Outline each Plasmodium falciparum-infected red blood cell.
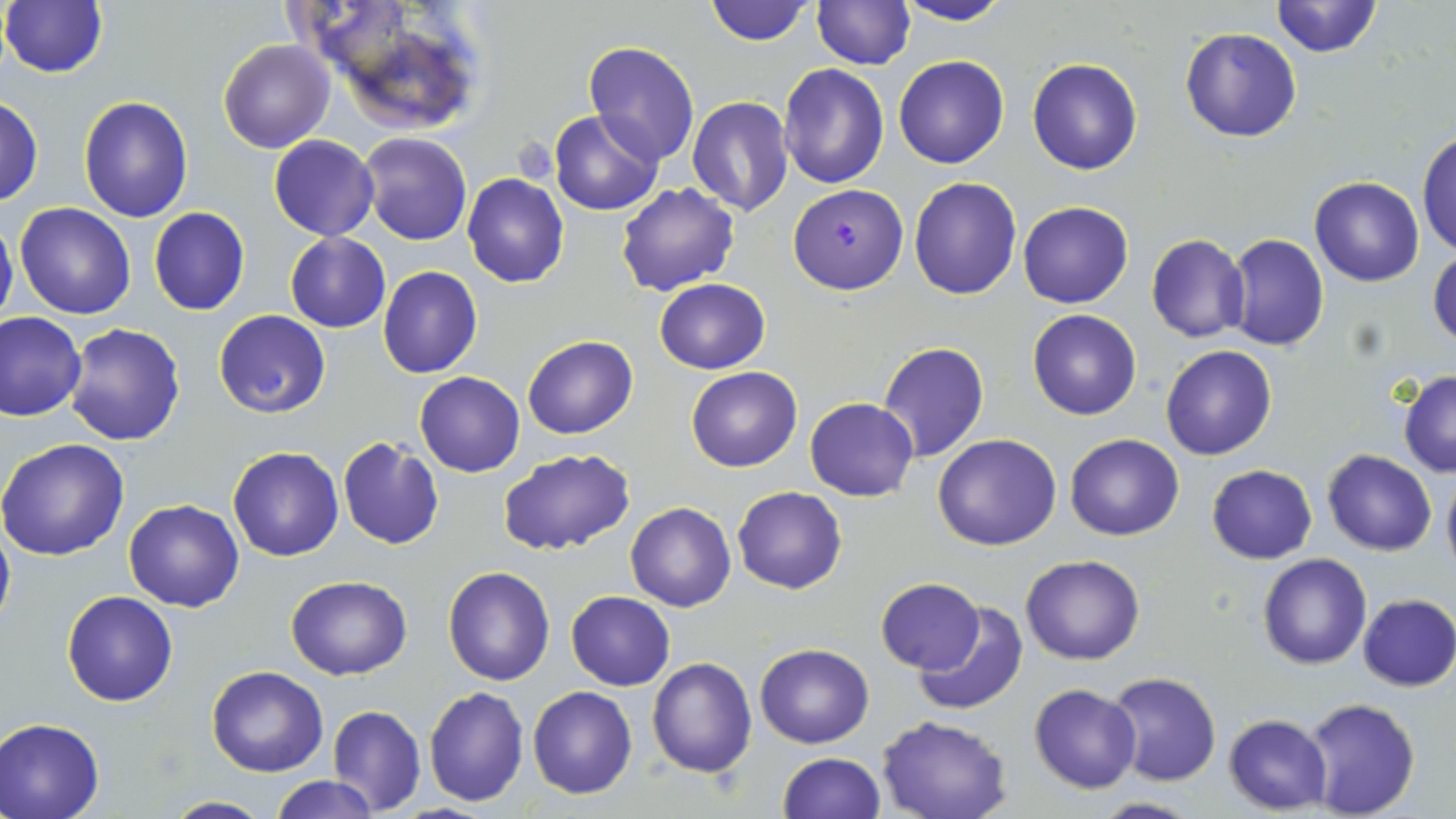

Approximate bounding boxes as (x1,y1)-(x2,y2) corner pairs in pixels.
Plasmodium falciparum-infected red blood cells: (787,183)-(908,294).

Summary:
  - Uninfected red blood cell locations: (704,0)-(815,46), (1269,0)-(1384,57), (895,1)-(1013,27), (1,2)-(108,78), (812,2)-(914,69), (315,6)-(492,135), (1180,26)-(1302,142), (218,39)-(334,153), (582,41)-(700,167), (893,56)-(1009,170), (1027,57)-(1143,175), (779,63)-(888,188), (0,95)-(44,206), (78,96)-(194,223), (685,97)-(795,218), (550,110)-(663,215), (1416,127)-(1456,259), (358,132)-(472,245), (269,135)-(379,240), (462,174)-(569,289), (908,175)-(1023,300), (1309,176)-(1425,286), (616,182)-(741,296), (14,201)-(137,320), (1018,201)-(1134,309), (148,208)-(251,316), (0,212)-(18,331), (285,232)-(390,331), (1146,234)-(1251,343), (1225,234)-(1330,351), (1429,246)-(1456,350), (378,267)-(483,379), (654,279)-(772,375), (1027,308)-(1141,420), (214,309)-(331,418), (0,311)-(85,421), (62,323)-(186,446), (521,335)-(638,439), (878,342)-(990,462), (1160,346)-(1278,461), (686,366)-(802,472), (1398,369)-(1456,477), (415,372)-(525,476), (805,397)-(918,502), (933,432)-(1061,550), (1064,432)-(1184,541), (336,436)-(444,550), (0,437)-(131,559), (227,447)-(344,561), (498,447)-(636,556), (1322,450)-(1438,556), (1206,464)-(1318,564), (1440,464)-(1456,580), (733,486)-(848,594), (124,498)-(244,611), (625,501)-(736,613), (0,514)-(14,634), (1020,553)-(1145,665), (1257,553)-(1371,670), (443,565)-(555,686), (285,574)-(412,680), (876,578)-(985,674), (62,591)-(178,706), (566,591)-(675,690), (1357,594)-(1456,692), (914,601)-(1029,718), (755,643)-(873,748), (647,656)-(757,777), (207,665)-(328,776), (1105,672)-(1221,787), (1029,683)-(1142,794), (424,685)-(530,807), (527,685)-(638,799), (1299,697)-(1423,818), (328,705)-(426,816), (876,715)-(1013,819), (1224,715)-(1332,813), (0,718)-(104,819), (778,751)-(884,818), (270,775)-(379,818), (161,795)-(272,818), (1086,796)-(1204,818)
  - Slide-level diagnosis: Plasmodium falciparum
  - Stain: May-Grünwald-Giemsa
  - Magnification: 1000x
  - Field of view: one of a larger specimen
  - Preparation: thin blood film
  - Image size: 1456×819 pixels
  - Modality: optical microscopy